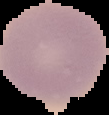
{
  "image_type": "segmented cell region on a black background",
  "image_size": "109×115 pixels",
  "preparation": "thin blood film",
  "result": "no malaria parasites seen"
}